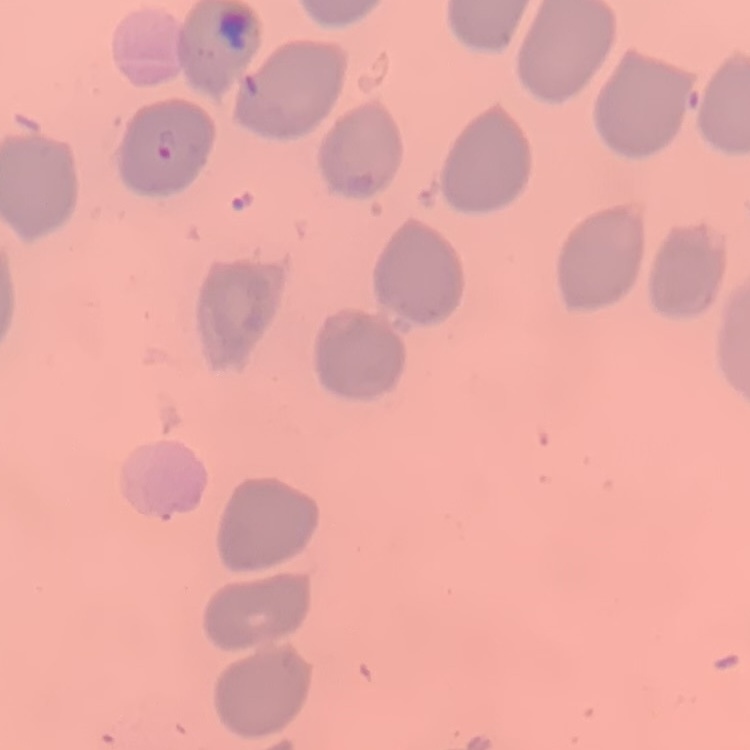 The erythrocytes exhibit no rouleaux formation. One tile cut from a larger photomicrograph. Thin blood film. Field's or Giemsa stain.